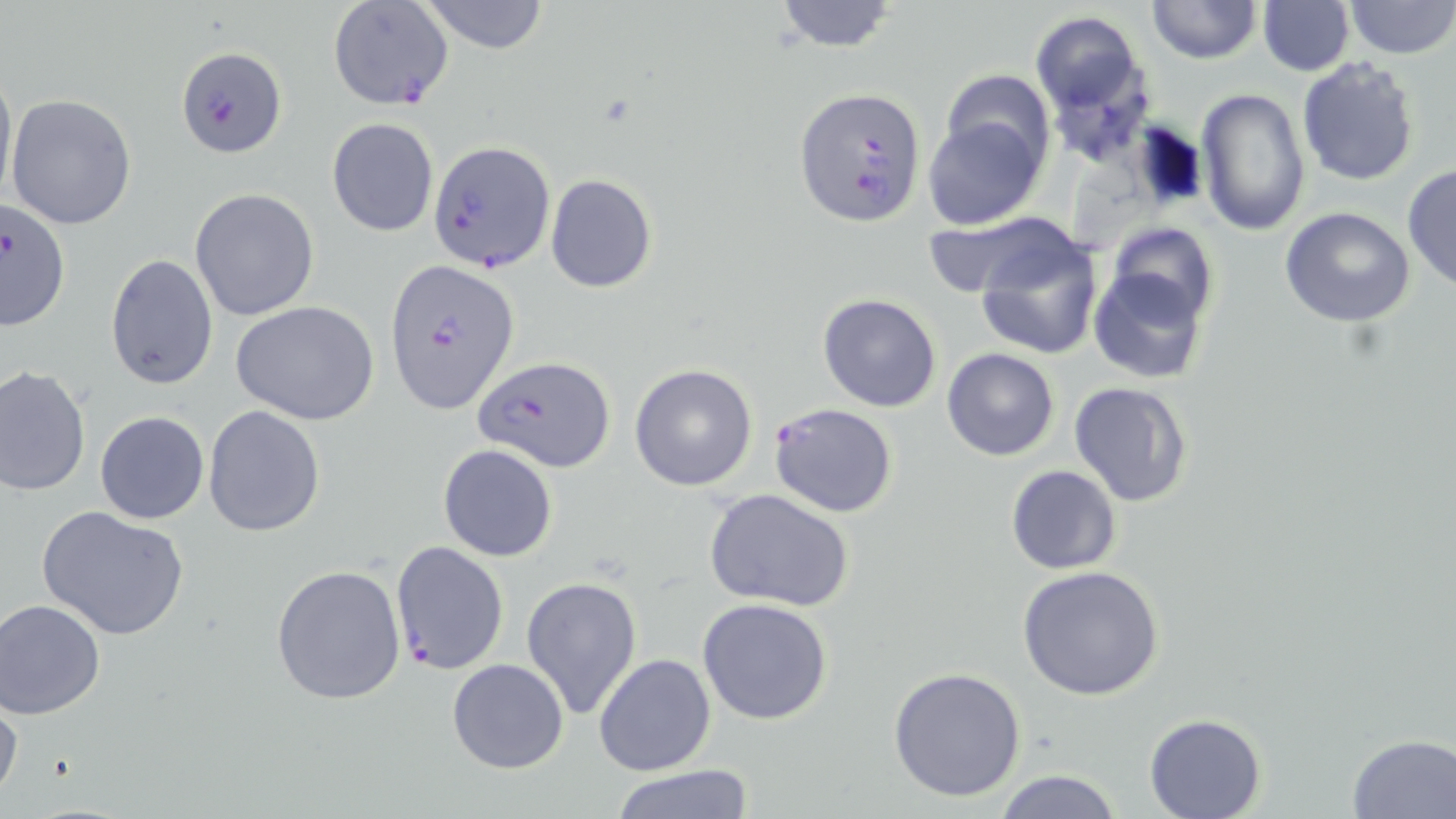

Summary:
  - Coordinate format: approximate bounding boxes as [x1, y1, x2, y2] in pixels
  - Uninfected red blood cell locations: [417, 0, 552, 54], [773, 0, 900, 51], [1146, 0, 1261, 64], [1344, 0, 1454, 58], [1257, 1, 1353, 76], [1030, 10, 1153, 158], [0, 56, 16, 214], [1296, 57, 1422, 187], [940, 70, 1054, 176], [1195, 87, 1309, 236], [6, 93, 136, 230], [924, 102, 1049, 232], [327, 117, 439, 237], [1401, 162, 1456, 294], [545, 173, 658, 293], [190, 188, 320, 322], [1279, 206, 1415, 327], [1102, 224, 1221, 329], [972, 227, 1103, 362], [105, 254, 218, 389], [1090, 265, 1211, 385], [818, 294, 941, 411], [233, 303, 379, 425], [941, 348, 1061, 461], [629, 364, 759, 491], [0, 366, 90, 500], [1067, 379, 1194, 508], [202, 405, 325, 535], [94, 411, 209, 524], [438, 443, 558, 562], [1006, 465, 1123, 575], [704, 487, 855, 611], [36, 505, 191, 640], [271, 564, 408, 705], [1018, 564, 1168, 702], [520, 574, 643, 721], [696, 596, 833, 726], [1, 600, 105, 720], [593, 652, 715, 775], [446, 659, 569, 774], [887, 665, 1028, 801], [0, 693, 23, 806], [1143, 713, 1268, 819], [1346, 733, 1455, 816], [607, 766, 756, 819], [992, 768, 1124, 819]
  - Plasmodium falciparum-infected red blood cell locations: [327, 2, 454, 110], [176, 46, 287, 156], [796, 86, 924, 223], [430, 140, 554, 274], [0, 196, 70, 328], [385, 257, 518, 416], [472, 356, 617, 472], [769, 402, 898, 518], [389, 541, 510, 674]
  - Slide-level diagnosis: Plasmodium falciparum
  - Stain: May-Grünwald-Giemsa
  - Preparation: thin blood smear
  - Field of view: single
  - Image size: 1456×819 pixels
  - Modality: optical microscopy
  - Magnification: 1000x